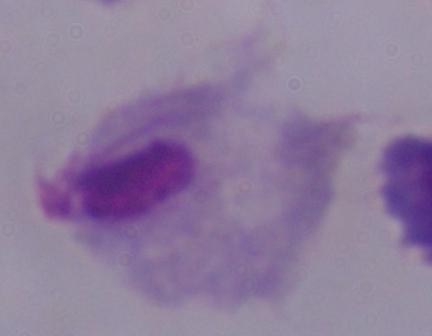
Summary:
  - Magnification: 1000x
  - Modality: photomicrograph
  - Identification: trichomonad